Classify this cell by malaria status.
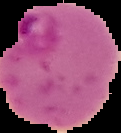
Parasitized.

From a thin blood film. Image is 121×133 pixels. The area outside the segmented cell region is set to black.